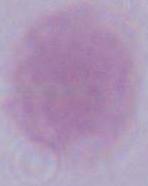 Captured at 1000x magnification. An erythrocyte is seen. Micrograph.